Assess this cell for malaria.
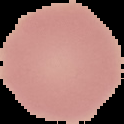

It is uninfected.

Image is 124×124 pixels. From a thin blood film. Cell region segmented out of the field of view; the surrounding area is masked to black.